Classify this cell by malaria status.
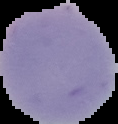

Uninfected.

{
  "image_type": "cell region segmented out of the field of view; surrounding area masked to black",
  "preparation": "thin blood film",
  "image_size": "118×124 pixels"
}